Identify the cell.
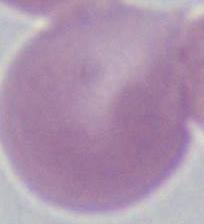

This is an erythrocyte.

1000x magnification. Photomicrograph.